Assess this cell for malaria.
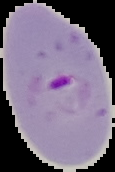

It is parasitized.

image_type: segmented cell region on a black background
preparation: thin blood smear
image_size: 115×172 pixels